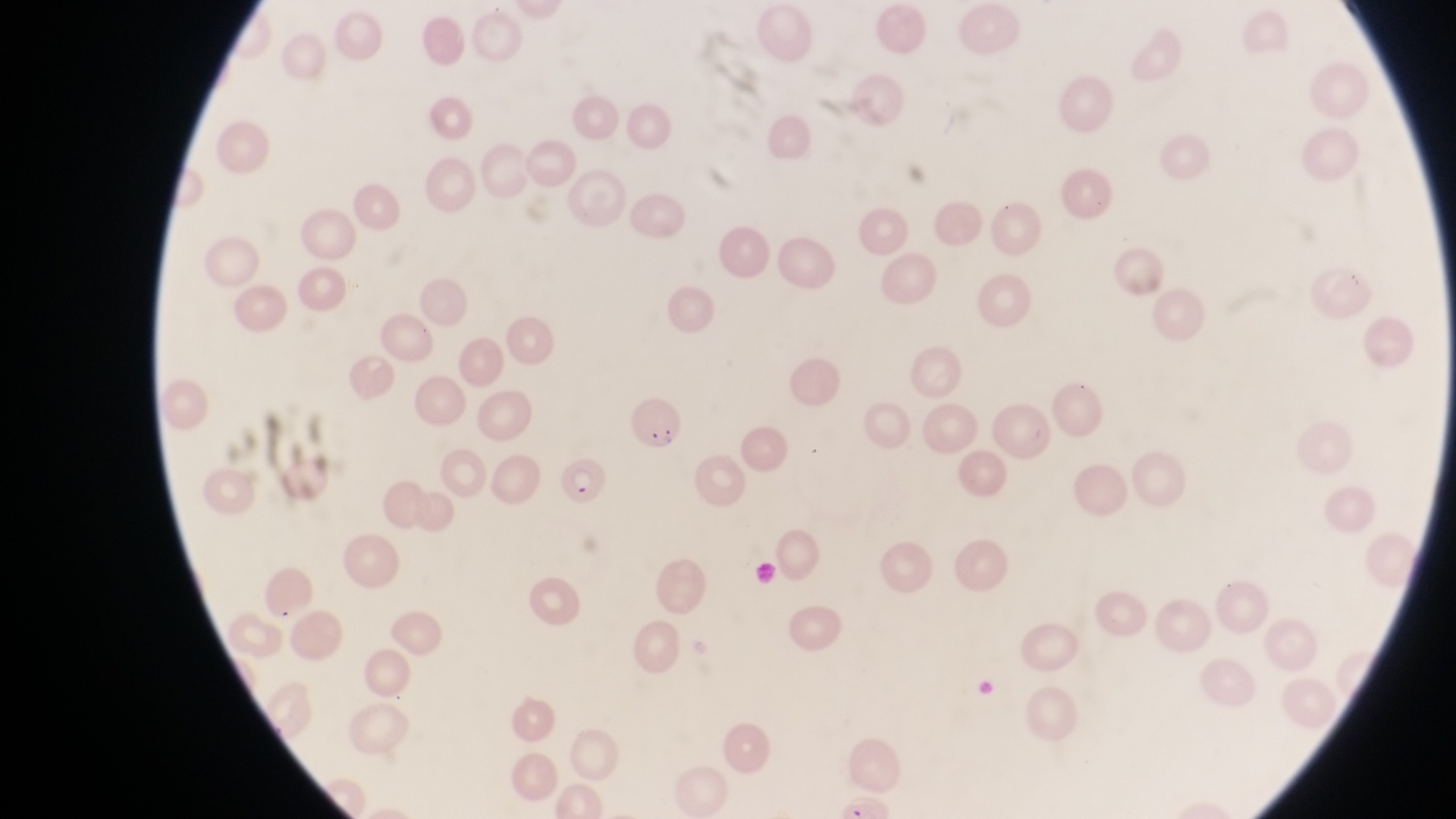 Approximate bounding boxes as (left, top, right, bottom) in pixels. Parasitised red blood cell locations: (623, 393, 679, 453), (555, 457, 608, 507). Single field of view. Image is 1456×819 pixels. At a magnification of 1000x. Collected in Uganda. Thin blood film. Captured by a smartphone held over the eyepiece of an Olympus CX-23 microscope.